State which parasite is depicted.
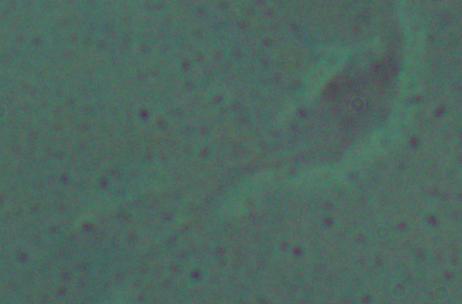

This is Leishmania.

modality = photomicrograph
magnification = 1000x